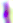
modality = photomicrograph
identification = Toxoplasma gondii
magnification = 400x